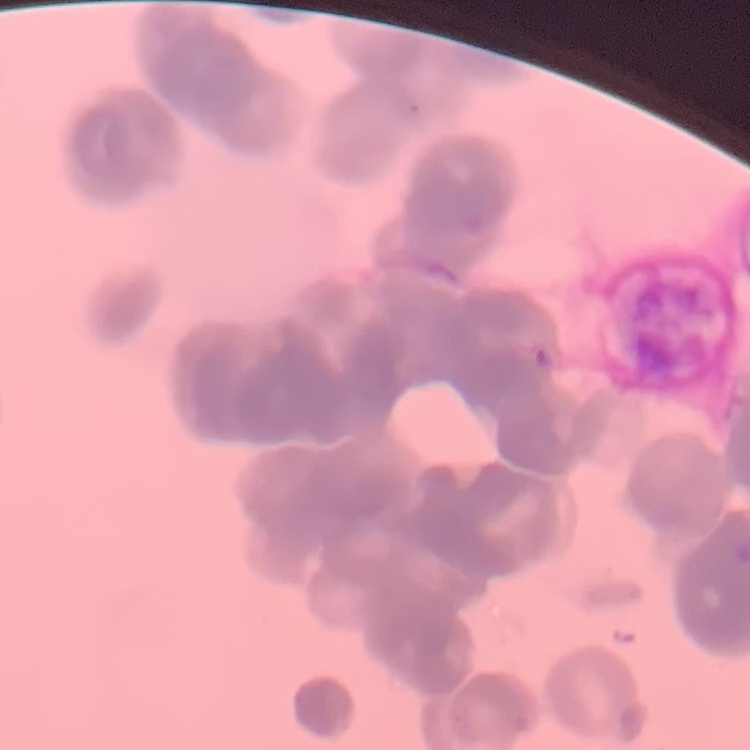

red blood cell morphology = rouleaux formation
preparation = thin blood smear
image type = one tile cut from a larger photomicrograph
stain = Field's or Giemsa